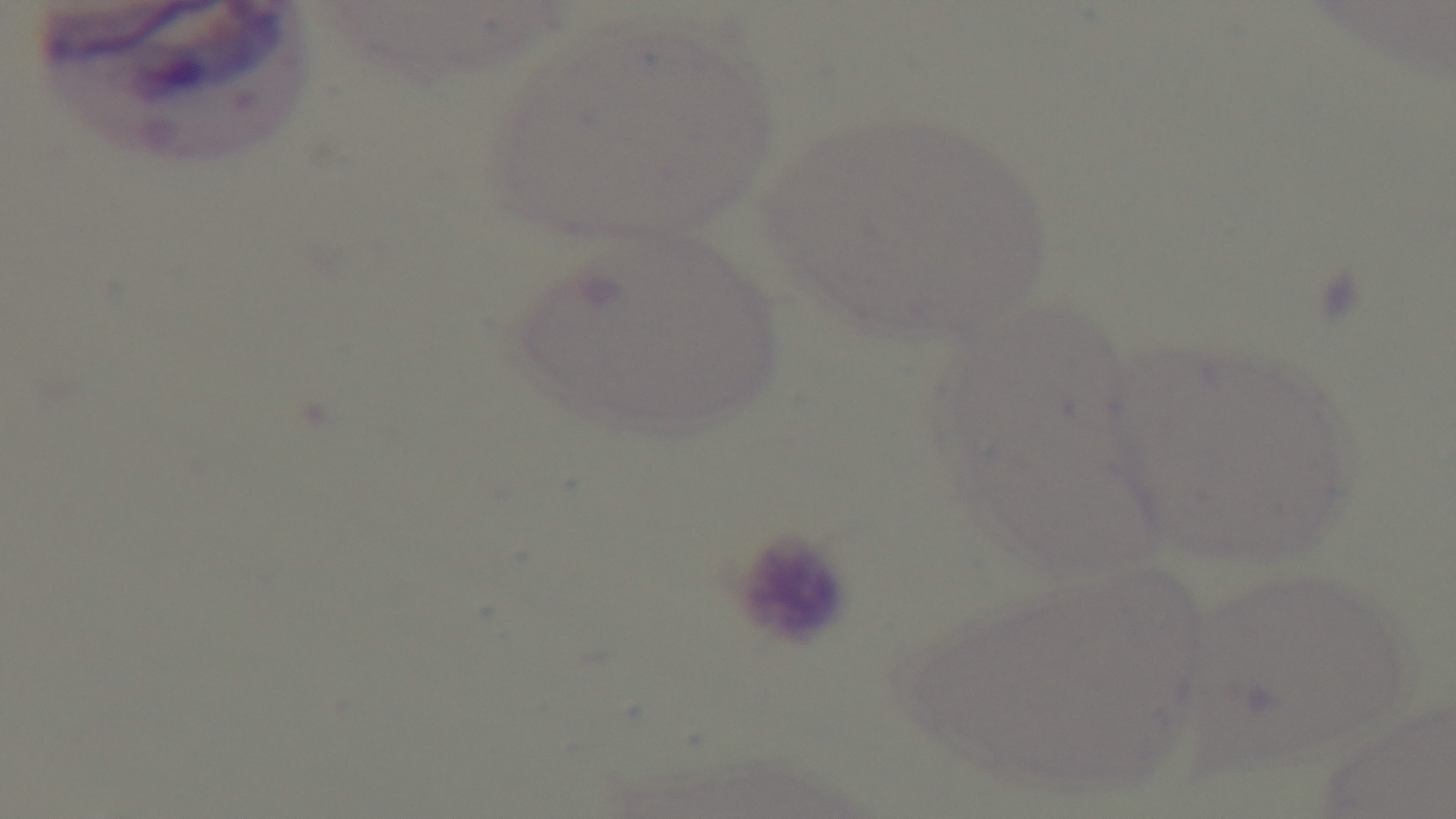
Summary:
  - Malaria status: negative
  - Preparation: thin
  - Stain: Giemsa
  - Modality: light microscopy
  - Field of view: one from the slide
  - Capture: mounted 4K digital camera
  - Objective: 100x oil immersion